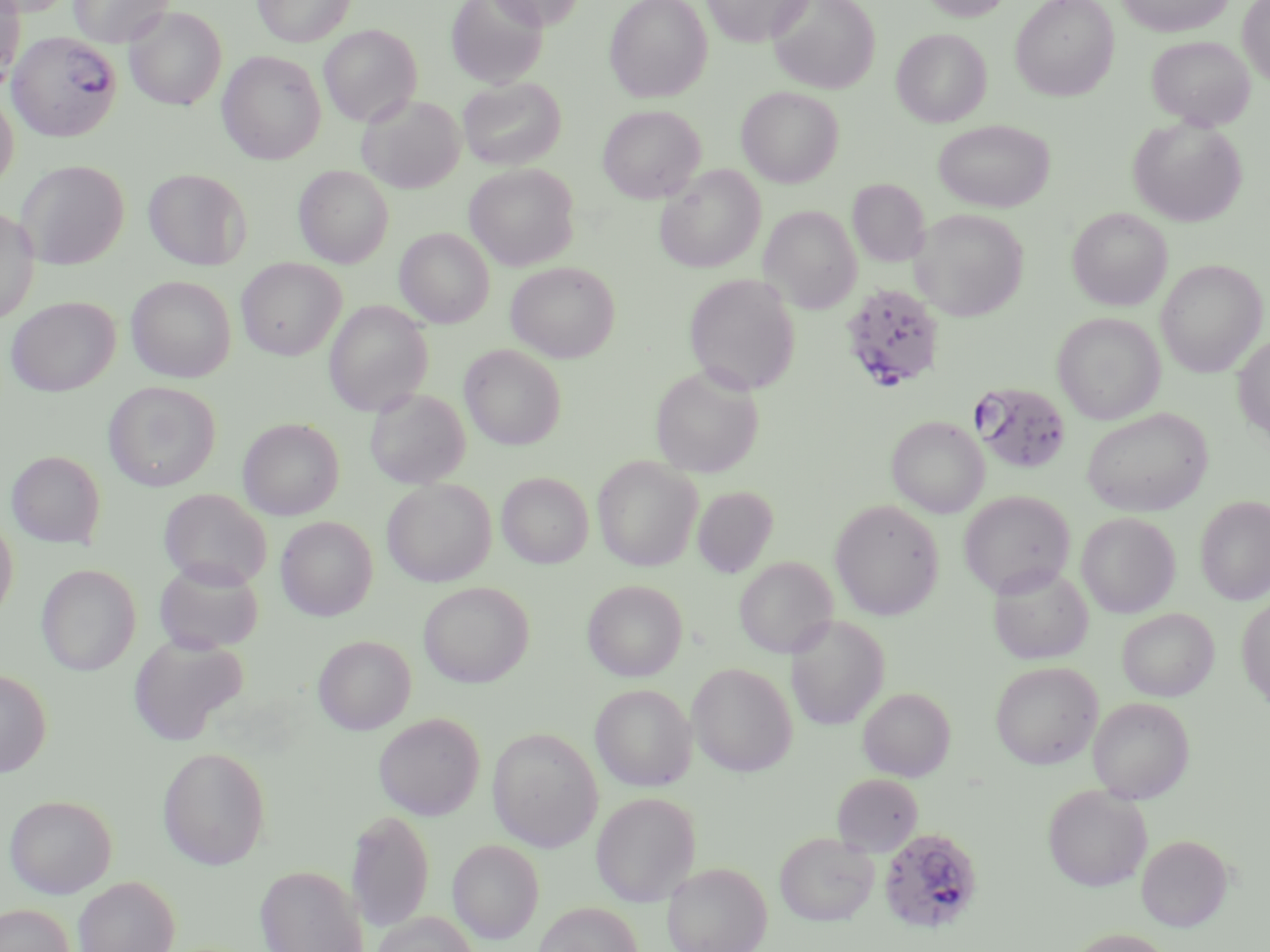
slide-level diagnosis = Plasmodium falciparum
field of view = single
modality = optical microscopy
Plasmodium falciparum-infected red blood cell locations = approximate bounding boxes as (x1,y1)-(x2,y2) corner pairs in pixels: (7,31)-(123,141), (839,283)-(946,395), (968,381)-(1072,476), (878,826)-(984,935)
preparation = thin blood film
magnification = 1000x
stain = May-Grünwald-Giemsa
image size = 1270×952 pixels
uninfected red blood cell locations = approximate bounding boxes as (x1,y1)-(x2,y2) corner pairs in pixels: (0,0)-(75,16), (68,0)-(173,48), (253,0)-(355,47), (446,0)-(548,88), (485,0)-(585,30), (604,0)-(713,102), (702,0)-(813,47), (768,0)-(880,94), (920,0)-(1012,21), (1010,0)-(1119,101), (1117,0)-(1234,37), (1237,0)-(1270,87), (0,3)-(25,90), (124,7)-(226,111), (319,24)-(422,127), (892,28)-(991,127), (1147,35)-(1255,130), (218,51)-(326,164), (458,77)-(566,171), (736,86)-(844,187), (0,90)-(19,190), (357,95)-(465,193), (598,105)-(705,203), (1128,117)-(1247,226), (933,119)-(1055,212), (16,160)-(129,269), (464,163)-(579,271), (294,165)-(394,267), (655,165)-(765,274), (143,168)-(251,270), (848,180)-(930,267), (759,205)-(861,314), (1067,207)-(1173,311), (0,208)-(40,324), (910,208)-(1029,321), (395,228)-(494,327), (237,258)-(346,360), (1156,259)-(1267,377), (507,261)-(620,363), (684,273)-(800,395), (126,276)-(236,383), (6,297)-(119,396), (324,301)-(433,415), (1052,312)-(1165,424), (1233,334)-(1270,442), (460,345)-(566,450), (650,365)-(764,478), (103,381)-(221,491), (365,388)-(470,489), (1082,408)-(1212,516), (887,416)-(988,518), (238,418)-(344,520), (7,450)-(105,548), (593,455)-(702,571), (497,472)-(593,568), (382,478)-(496,586), (692,486)-(778,576), (159,488)-(272,590), (958,490)-(1075,598), (1196,495)-(1270,605), (829,499)-(945,620), (1076,512)-(1180,618), (0,516)-(18,623), (276,516)-(377,621), (735,557)-(837,659), (154,559)-(264,654), (988,563)-(1093,665), (36,564)-(141,675), (582,579)-(687,681), (419,581)-(533,688), (1237,594)-(1270,711), (1117,608)-(1219,701), (786,614)-(889,730), (128,634)-(248,746), (313,635)-(416,734), (688,662)-(797,777), (991,662)-(1102,770), (0,669)-(51,777), (590,684)-(697,792), (858,687)-(955,781), (1088,697)-(1195,803), (373,712)-(485,820), (487,727)-(603,851), (158,745)-(271,869), (832,774)-(923,856), (1043,784)-(1152,892), (591,791)-(701,905), (4,793)-(117,898), (346,807)-(434,932), (774,832)-(879,926), (1136,834)-(1233,931), (447,839)-(544,943), (661,861)-(772,952), (255,864)-(367,952), (73,876)-(180,952), (532,902)-(643,952), (0,903)-(76,952), (370,912)-(479,952), (1064,928)-(1175,952)